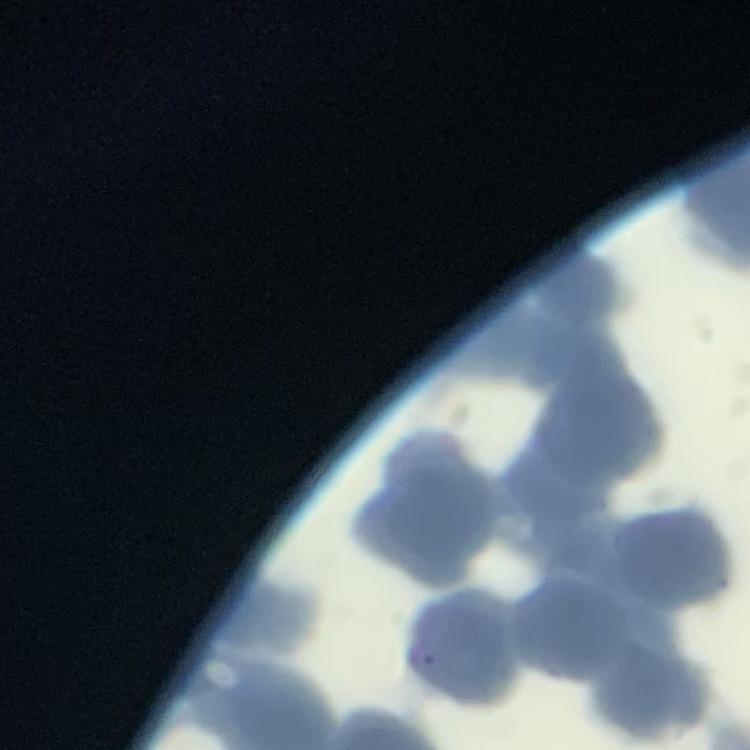
red_blood_cell_morphology: rouleaux formation
image_type: one tile cut from a larger photomicrograph
stain: Field's or Giemsa
preparation: thin blood film